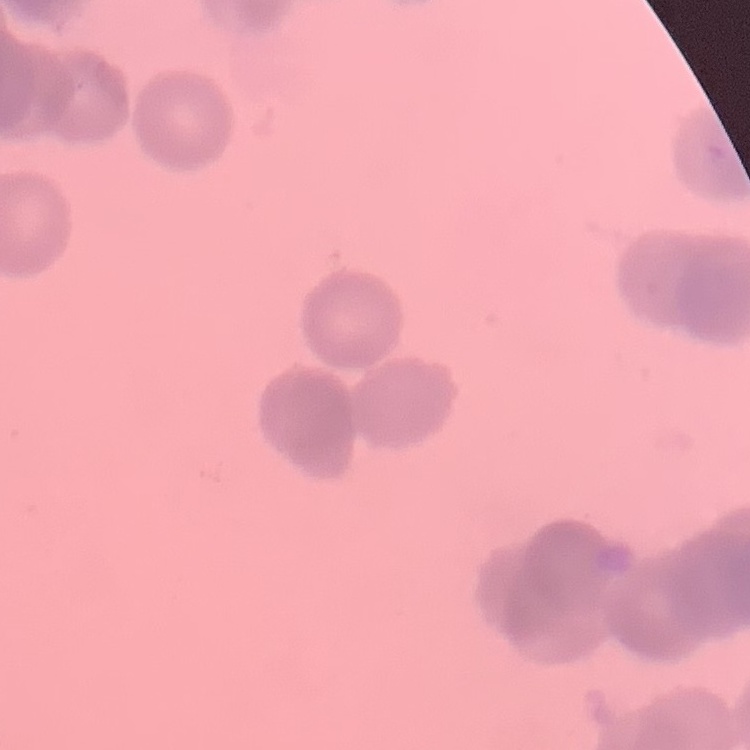

Summary:
  - Red blood cell morphology: rouleaux formation
  - Image type: square crop of a larger photomicrograph
  - Preparation: thin peripheral smear
  - Stain: Field's or Giemsa